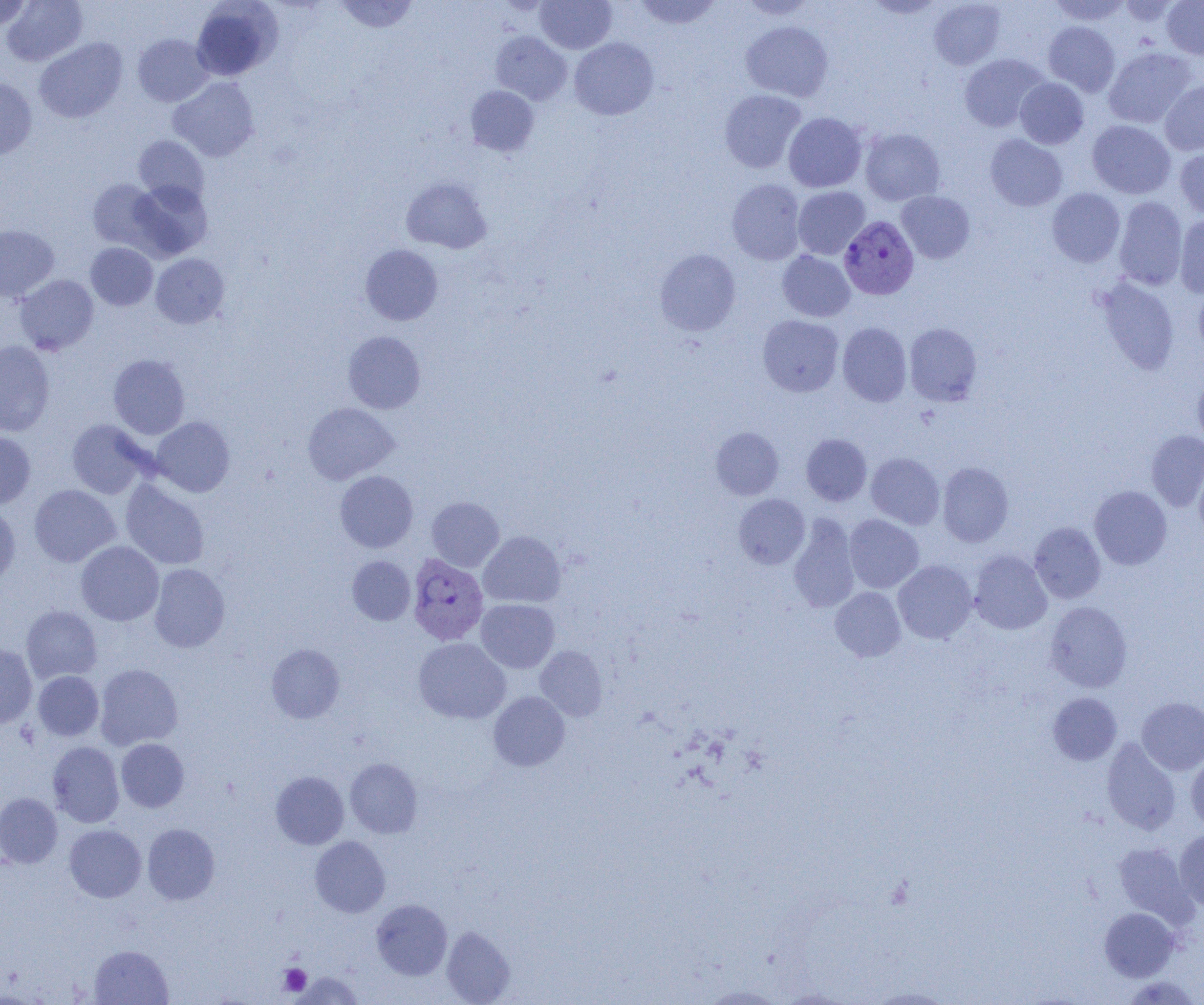

Approximate bounding boxes as named x1/y1/x2/y2 corners in pixels. Plasmodium vivax-infected red blood cell locations: (x1=839, y1=216, x2=919, y2=299), (x1=407, y1=554, x2=489, y2=646). Platelet locations: (x1=279, y1=964, x2=311, y2=996). Uninfected red blood cell locations: (x1=2, y1=0, x2=88, y2=66), (x1=334, y1=0, x2=419, y2=34), (x1=535, y1=0, x2=617, y2=53), (x1=633, y1=0, x2=723, y2=30), (x1=1049, y1=0, x2=1132, y2=26), (x1=1119, y1=0, x2=1179, y2=26), (x1=1161, y1=0, x2=1204, y2=59), (x1=0, y1=1, x2=33, y2=30), (x1=191, y1=1, x2=282, y2=80), (x1=738, y1=1, x2=818, y2=19), (x1=862, y1=1, x2=946, y2=18), (x1=929, y1=1, x2=1005, y2=69), (x1=741, y1=21, x2=833, y2=101), (x1=1043, y1=21, x2=1120, y2=96), (x1=491, y1=31, x2=572, y2=105), (x1=132, y1=33, x2=214, y2=107), (x1=570, y1=37, x2=658, y2=120), (x1=35, y1=38, x2=127, y2=123), (x1=1103, y1=47, x2=1196, y2=128), (x1=959, y1=53, x2=1049, y2=131), (x1=168, y1=77, x2=259, y2=162), (x1=0, y1=78, x2=37, y2=159), (x1=1015, y1=78, x2=1089, y2=149), (x1=1160, y1=80, x2=1204, y2=155), (x1=465, y1=86, x2=539, y2=156), (x1=719, y1=89, x2=806, y2=173), (x1=783, y1=112, x2=867, y2=192), (x1=1087, y1=120, x2=1175, y2=198), (x1=860, y1=128, x2=945, y2=206), (x1=985, y1=134, x2=1067, y2=211), (x1=133, y1=136, x2=209, y2=205), (x1=1175, y1=147, x2=1204, y2=219), (x1=401, y1=177, x2=492, y2=253), (x1=87, y1=179, x2=163, y2=251), (x1=128, y1=179, x2=212, y2=260), (x1=727, y1=179, x2=806, y2=265), (x1=793, y1=186, x2=870, y2=259), (x1=1047, y1=188, x2=1125, y2=267), (x1=897, y1=191, x2=975, y2=263), (x1=1114, y1=197, x2=1188, y2=289), (x1=1175, y1=214, x2=1204, y2=298), (x1=0, y1=224, x2=60, y2=302), (x1=86, y1=242, x2=158, y2=310), (x1=360, y1=244, x2=443, y2=325), (x1=654, y1=248, x2=741, y2=336), (x1=777, y1=250, x2=855, y2=321), (x1=151, y1=253, x2=230, y2=328), (x1=15, y1=275, x2=99, y2=355), (x1=1096, y1=276, x2=1180, y2=374), (x1=1192, y1=286, x2=1204, y2=360), (x1=758, y1=315, x2=844, y2=397), (x1=837, y1=322, x2=912, y2=406), (x1=904, y1=322, x2=982, y2=405), (x1=342, y1=331, x2=426, y2=413), (x1=0, y1=341, x2=55, y2=436), (x1=108, y1=354, x2=190, y2=439), (x1=1192, y1=374, x2=1204, y2=449), (x1=303, y1=402, x2=399, y2=484), (x1=151, y1=417, x2=235, y2=497), (x1=67, y1=420, x2=152, y2=498), (x1=711, y1=426, x2=784, y2=500), (x1=1146, y1=430, x2=1204, y2=511), (x1=0, y1=431, x2=36, y2=509), (x1=801, y1=434, x2=872, y2=506), (x1=866, y1=452, x2=945, y2=529), (x1=1194, y1=458, x2=1204, y2=541), (x1=937, y1=462, x2=1013, y2=546), (x1=335, y1=470, x2=418, y2=553), (x1=120, y1=479, x2=210, y2=569), (x1=29, y1=484, x2=120, y2=567), (x1=1089, y1=485, x2=1172, y2=569), (x1=733, y1=494, x2=810, y2=568), (x1=427, y1=497, x2=504, y2=572), (x1=0, y1=502, x2=20, y2=587), (x1=789, y1=514, x2=860, y2=613), (x1=844, y1=514, x2=924, y2=593), (x1=1029, y1=522, x2=1106, y2=603), (x1=478, y1=531, x2=565, y2=607), (x1=76, y1=541, x2=163, y2=626), (x1=969, y1=549, x2=1052, y2=634), (x1=347, y1=556, x2=415, y2=626), (x1=893, y1=560, x2=977, y2=643), (x1=149, y1=563, x2=230, y2=652), (x1=830, y1=587, x2=906, y2=661), (x1=476, y1=599, x2=559, y2=672), (x1=1045, y1=601, x2=1132, y2=692), (x1=21, y1=605, x2=102, y2=683), (x1=414, y1=637, x2=510, y2=724), (x1=0, y1=643, x2=37, y2=728), (x1=266, y1=644, x2=344, y2=723), (x1=535, y1=645, x2=607, y2=721), (x1=95, y1=664, x2=183, y2=750), (x1=33, y1=671, x2=104, y2=741), (x1=488, y1=691, x2=570, y2=771), (x1=1048, y1=692, x2=1121, y2=765), (x1=1136, y1=697, x2=1204, y2=775), (x1=116, y1=738, x2=189, y2=812), (x1=1102, y1=738, x2=1181, y2=835), (x1=48, y1=741, x2=124, y2=827), (x1=1186, y1=755, x2=1204, y2=832), (x1=345, y1=758, x2=423, y2=838), (x1=270, y1=771, x2=349, y2=849), (x1=0, y1=792, x2=63, y2=868), (x1=64, y1=824, x2=146, y2=902), (x1=142, y1=824, x2=219, y2=904), (x1=1174, y1=829, x2=1204, y2=911), (x1=310, y1=836, x2=390, y2=917), (x1=1113, y1=842, x2=1194, y2=923), (x1=371, y1=899, x2=452, y2=979), (x1=1100, y1=907, x2=1178, y2=981), (x1=441, y1=926, x2=515, y2=1004), (x1=90, y1=945, x2=173, y2=1004), (x1=292, y1=971, x2=363, y2=1004), (x1=1121, y1=975, x2=1201, y2=1005), (x1=702, y1=985, x2=785, y2=1004), (x1=868, y1=987, x2=955, y2=1004). Slide-level diagnosis: Plasmodium vivax. Image is 1204×1005 pixels. Optical microscopy. One field of a larger specimen. 1000x magnification. Thin blood smear.